State which parasite is depicted.
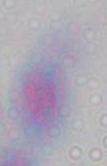
This is Toxoplasma gondii.

Micrograph. 1000x magnification.